Assess this cell for malaria.
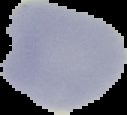
It is parasitized.

The area outside the segmented cell region is set to black. From a thin blood smear. Image is 127×115 pixels.